Locate leukocytes (white blood cells).
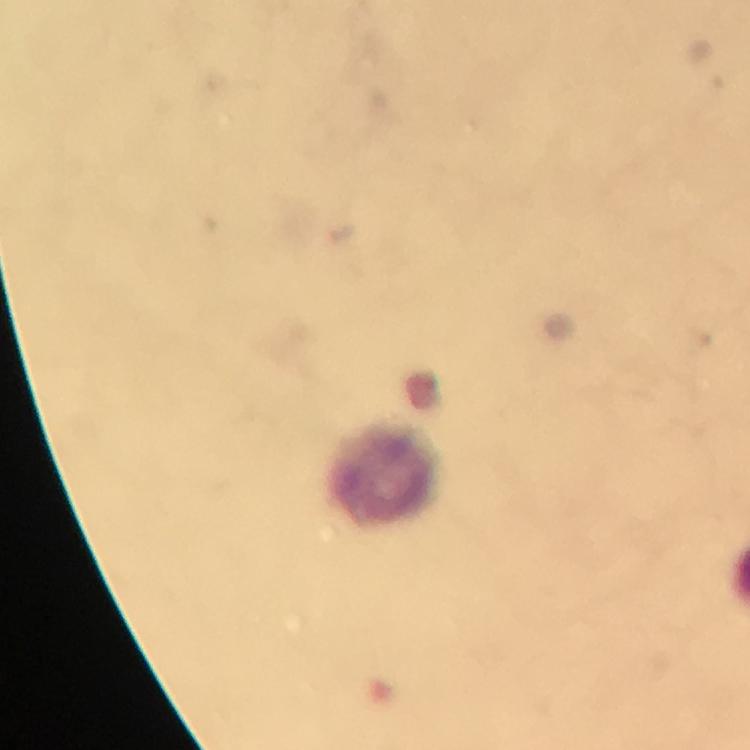

Approximate centers as [x, y] in pixels.
Leukocytes: [387, 475].

Cropped region of a single field of view. Giemsa-stained preparation. Smartphone photograph taken through a microscope. From a malaria diagnostic workup. Malaria parasites: none seen. Image is 750×750 pixels. At 100x magnification. Thick smear. Immersion oil was used.